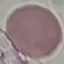 Malaria status: uninfected. Automatically extracted cell patch, resized to 64 × 64 pixels. Acquired by smartphone through the microscope eyepiece. Giemsa-stained preparation. Thin blood film.